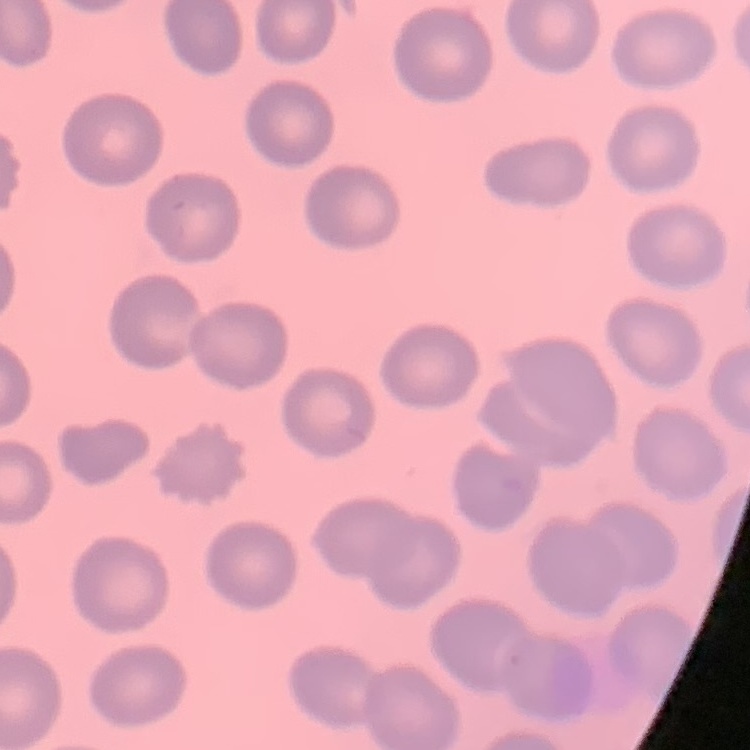
erythrocyte_morphology: no rouleaux formation
stain: Field's or Giemsa
preparation: thin peripheral smear
image_type: one tile cut from a larger photomicrograph